Locate the red blood cells and classify each one as Plasmodium falciparum-infected, uninfected, or of indeterminate infection status.
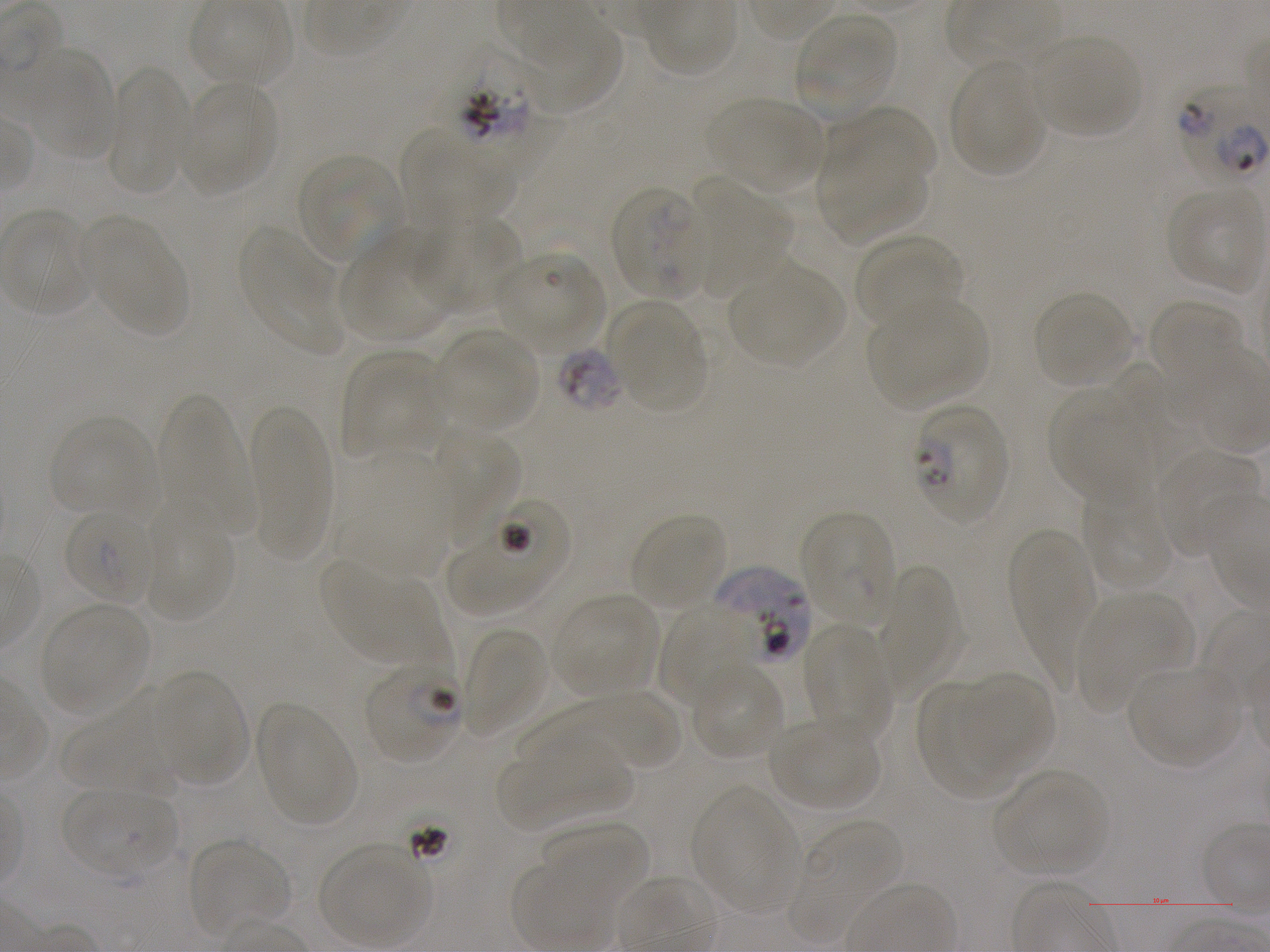
Approximate bounding boxes as [x1, y1, x2, y2] in pixels. Not every red blood cell is marked. A life-cycle stage — or a range of stages, where the recorded stages span more than one — follows each staged infected red blood cell.
Infected red blood cells: [448, 44, 540, 155]; [1174, 80, 1270, 197]; [611, 187, 706, 298]; [910, 403, 1010, 525] late ring; [446, 498, 570, 618]; [63, 508, 158, 605]; [713, 565, 813, 668]; [365, 661, 463, 764] ring.
Red blood cells of indeterminate infection status: [557, 348, 624, 412].
Uninfected red blood cells: [522, 13, 627, 116], [794, 13, 899, 121], [1030, 36, 1141, 138], [22, 48, 117, 162], [948, 59, 1047, 178], [107, 63, 190, 196], [181, 81, 277, 193], [711, 97, 824, 193], [827, 108, 935, 193], [401, 129, 516, 232], [820, 148, 930, 244], [295, 152, 404, 264], [689, 178, 792, 293], [1166, 188, 1266, 290], [4, 211, 97, 317], [413, 214, 525, 316], [89, 225, 190, 338], [238, 227, 343, 354], [338, 231, 452, 344], [854, 234, 962, 331], [496, 251, 602, 352], [732, 265, 843, 368], [1034, 291, 1136, 388], [870, 297, 989, 407], [1147, 298, 1244, 387], [610, 303, 706, 411], [438, 329, 540, 432], [342, 351, 444, 459], [1102, 362, 1200, 484], [1049, 389, 1146, 506], [157, 394, 252, 533], [248, 400, 333, 557], [50, 416, 157, 518], [438, 426, 520, 547], [1158, 448, 1261, 554], [341, 453, 453, 576], [1081, 489, 1170, 592], [800, 510, 897, 628], [631, 512, 727, 612], [143, 515, 235, 623], [1010, 528, 1095, 687], [321, 560, 436, 666], [875, 565, 960, 697], [1075, 591, 1189, 707], [554, 594, 659, 699], [659, 602, 754, 709], [39, 604, 152, 717], [460, 626, 549, 736], [803, 626, 892, 737], [690, 662, 784, 762], [1128, 666, 1238, 768], [154, 671, 251, 787], [961, 672, 1054, 779], [919, 681, 1014, 802], [549, 693, 682, 771], [64, 695, 179, 795], [256, 703, 358, 826], [769, 720, 882, 813], [501, 741, 635, 832], [994, 770, 1110, 878], [693, 786, 800, 915], [62, 787, 177, 880], [793, 821, 902, 929], [541, 822, 650, 915], [188, 839, 291, 937], [319, 844, 428, 946].

objective = 100x, oil immersion, numerical aperture 1.25
stain = Giemsa
image size = 1270×952 pixels
donor blood group = A+
field of view = one from this slide
preparation = thin blood smear
culture = in-vitro Plasmodium falciparum strain NF54, static